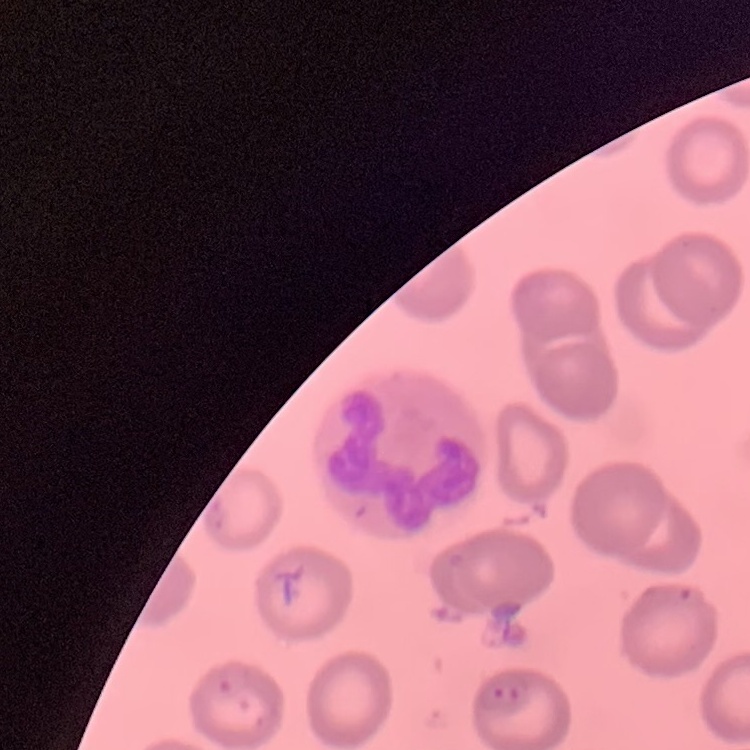
{
  "erythrocyte_morphology": "no rouleaux formation",
  "stain": "Field's or Giemsa",
  "preparation": "thin peripheral smear",
  "image_type": "square crop of a larger photomicrograph"
}